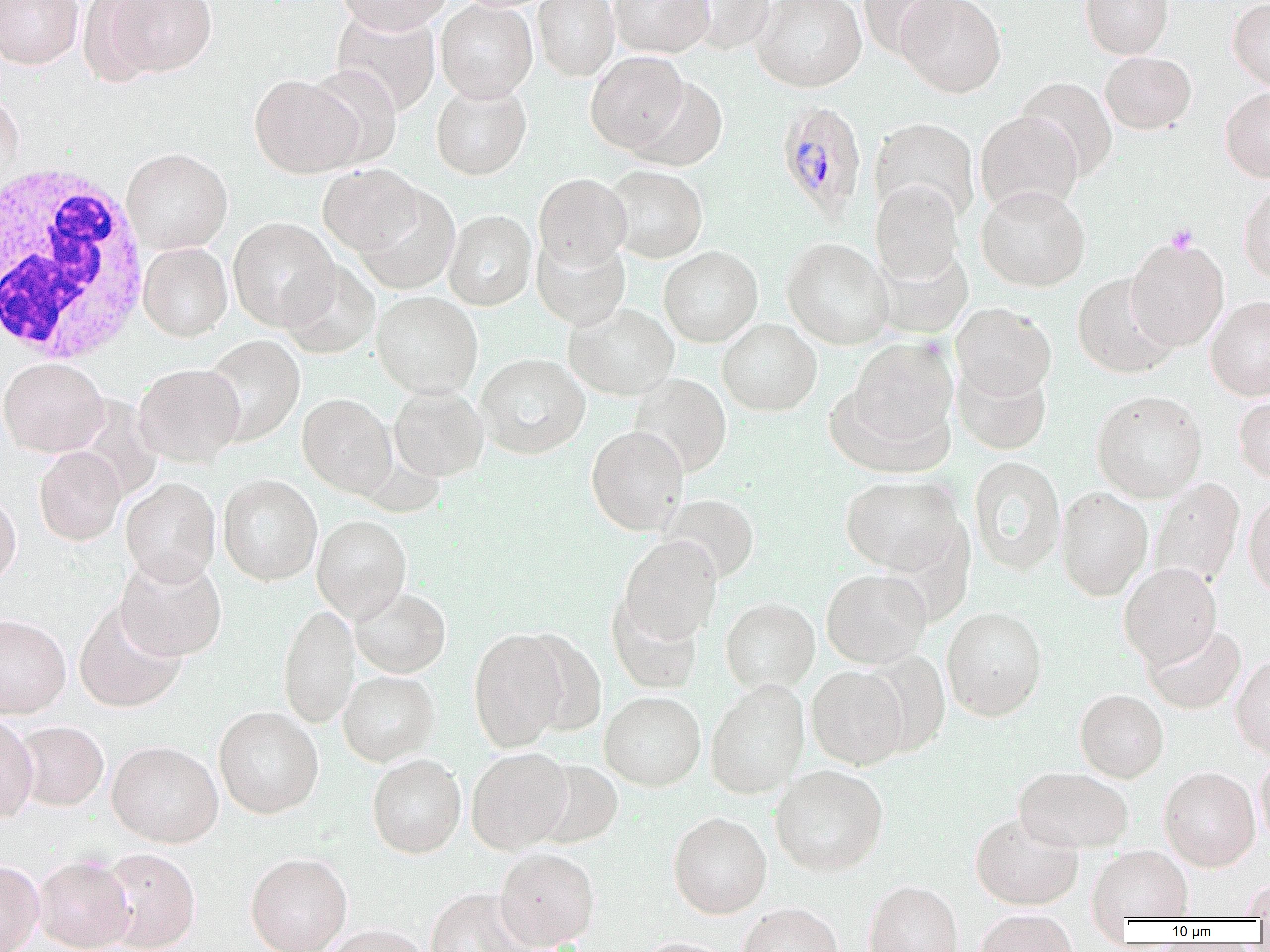
Summary:
  - Coordinate format: approximate bounding boxes as [x1, y1, x2, y2] in pixels
  - Platelet locations: [1165, 224, 1198, 254]
  - Uninfected red blood cell locations: [0, 0, 84, 69], [77, 0, 166, 87], [99, 0, 218, 78], [336, 0, 453, 35], [435, 0, 537, 102], [532, 0, 619, 81], [608, 0, 714, 58], [680, 0, 776, 54], [752, 0, 867, 92], [894, 0, 1006, 98], [1080, 0, 1174, 59], [1228, 0, 1270, 90], [856, 1, 960, 59], [331, 8, 441, 115], [586, 51, 689, 153], [1100, 51, 1196, 134], [305, 64, 403, 168], [249, 73, 363, 177], [628, 76, 728, 171], [1016, 76, 1118, 180], [430, 81, 532, 180], [1220, 86, 1270, 181], [0, 91, 24, 196], [975, 111, 1082, 213], [869, 118, 980, 224], [121, 147, 232, 254], [318, 164, 423, 256], [606, 165, 708, 262], [534, 173, 631, 269], [870, 180, 964, 285], [1238, 183, 1270, 284], [354, 184, 460, 294], [976, 186, 1091, 291], [443, 209, 536, 310], [228, 217, 339, 331], [531, 234, 630, 330], [781, 237, 894, 349], [1125, 238, 1229, 350], [138, 242, 232, 341], [872, 244, 974, 338], [658, 246, 763, 346], [280, 260, 380, 358], [1072, 274, 1179, 379], [371, 291, 483, 399], [1205, 296, 1270, 400], [564, 303, 680, 401], [951, 303, 1056, 399], [718, 318, 822, 415], [201, 334, 305, 446], [845, 337, 959, 455], [475, 354, 590, 459], [0, 357, 108, 457], [952, 362, 1052, 455], [134, 363, 245, 466], [628, 374, 732, 476], [389, 386, 489, 481], [1091, 390, 1207, 502], [1233, 393, 1270, 484], [297, 394, 397, 498], [586, 425, 689, 535], [34, 446, 126, 545], [968, 456, 1066, 575], [218, 474, 322, 585], [840, 475, 966, 576], [120, 478, 221, 586], [1149, 478, 1244, 591], [1055, 486, 1153, 601], [0, 490, 21, 587], [1244, 491, 1270, 598], [659, 493, 760, 584], [312, 514, 412, 622], [619, 535, 722, 644], [115, 554, 227, 661], [1118, 563, 1222, 668], [821, 568, 931, 669], [350, 587, 451, 678], [606, 593, 703, 693], [721, 597, 820, 694], [74, 602, 187, 712], [278, 604, 359, 728], [941, 606, 1048, 721], [0, 614, 71, 718], [1144, 623, 1246, 713], [468, 628, 570, 751], [517, 630, 608, 737], [859, 648, 950, 757], [1231, 655, 1270, 759], [806, 665, 909, 769], [338, 670, 440, 765], [705, 680, 809, 799], [1075, 689, 1169, 782], [599, 691, 706, 790], [213, 706, 324, 818], [0, 713, 38, 822], [14, 721, 109, 810], [106, 740, 223, 847], [466, 746, 572, 854], [1254, 750, 1270, 849], [367, 754, 466, 858], [531, 758, 623, 848], [770, 764, 889, 876], [1014, 766, 1134, 853], [1159, 766, 1260, 871], [668, 811, 772, 918], [970, 811, 1084, 910], [1088, 845, 1193, 921], [98, 847, 201, 951], [493, 847, 600, 949], [245, 852, 352, 952], [33, 854, 135, 952], [0, 860, 44, 952], [1241, 878, 1270, 919], [863, 880, 963, 952], [425, 888, 532, 952], [737, 903, 843, 952], [975, 909, 1078, 952], [321, 924, 429, 952], [637, 937, 738, 952]
  - Plasmodium malariae-infected red blood cell locations: [776, 99, 867, 220]
  - White blood cell locations: [0, 161, 153, 365]
  - Slide-level diagnosis: Plasmodium malariae
  - Preparation: thin blood smear
  - Field of view: one of a larger specimen
  - Magnification: 1000x
  - Image size: 1270×952 pixels
  - Modality: optical microscopy